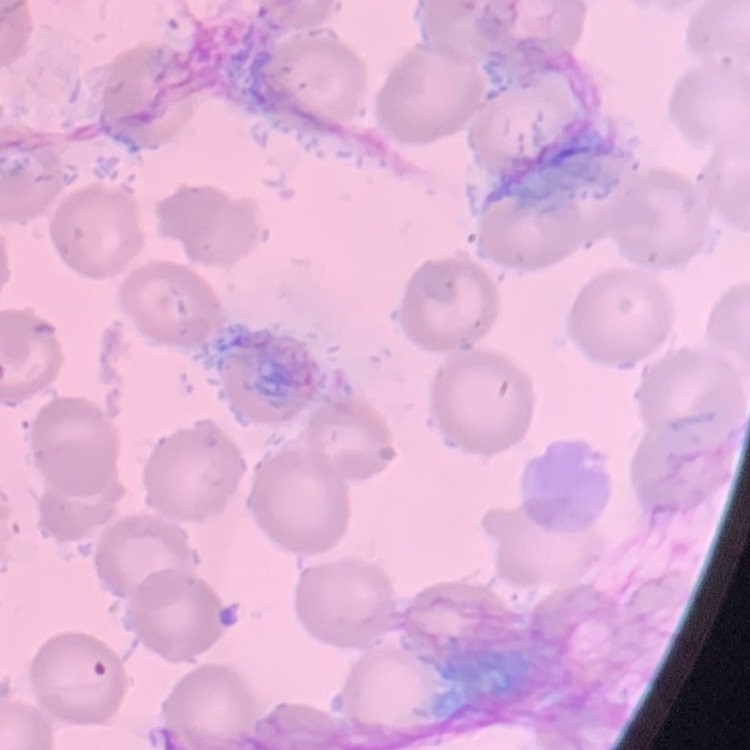

erythrocyte_morphology: no rouleaux formation
preparation: thin blood smear
image_type: one tile cut from a larger photomicrograph
stain: Field's or Giemsa